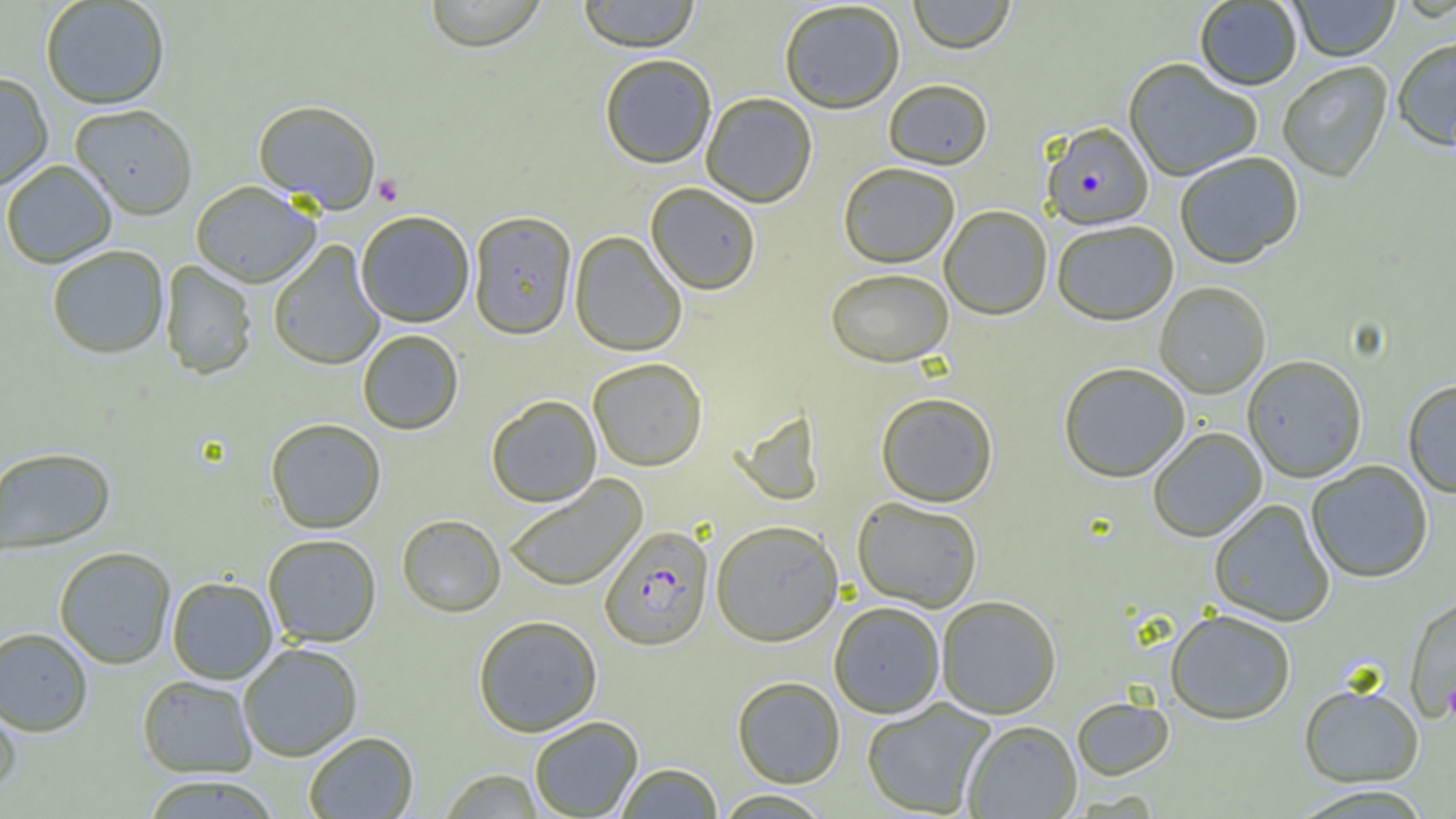
Summary:
  - Coordinate format: approximate bounding boxes as (x1,y1)-(x2,y2) corner pairs in pixels
  - Plasmodium falciparum-infected red blood cell locations: (1042,123)-(1154,232), (600,526)-(714,652)
  - Platelet locations: (373,173)-(404,207), (1442,680)-(1456,723)
  - Uninfected red blood cell locations: (423,0)-(548,53), (576,0)-(701,54), (908,0)-(1016,56), (1290,0)-(1400,63), (40,1)-(170,111), (779,2)-(906,116), (1194,2)-(1302,92), (1393,40)-(1456,155), (600,56)-(716,170), (1123,60)-(1262,182), (1278,63)-(1393,184), (0,73)-(53,192), (884,82)-(993,172), (701,94)-(817,209), (252,100)-(382,213), (70,106)-(197,221), (1175,153)-(1304,269), (1,161)-(117,269), (838,165)-(960,270), (191,183)-(320,289), (645,184)-(761,298), (940,207)-(1052,322), (356,212)-(474,328), (468,213)-(577,342), (1052,222)-(1179,328), (569,232)-(687,358), (268,241)-(385,371), (47,246)-(169,360), (160,261)-(257,381), (825,270)-(953,369), (1155,283)-(1270,400), (357,330)-(464,435), (1242,356)-(1367,484), (588,359)-(707,472), (1058,364)-(1190,483), (1402,380)-(1456,499), (875,394)-(998,508), (486,395)-(602,508), (733,411)-(824,508), (265,418)-(386,534), (1148,428)-(1267,543), (1,447)-(116,556), (1307,461)-(1433,584), (504,475)-(648,592), (852,498)-(982,613), (1209,499)-(1335,627), (397,515)-(506,618), (710,521)-(843,648), (263,534)-(382,648), (54,547)-(176,669), (167,577)-(278,684), (1404,593)-(1456,724), (936,597)-(1062,719), (829,602)-(945,718), (1165,611)-(1296,726), (473,616)-(602,738), (0,627)-(93,737), (238,643)-(363,762), (137,675)-(257,778), (732,676)-(845,789), (1299,685)-(1424,788), (0,696)-(22,798), (1072,697)-(1174,781), (861,699)-(995,817), (529,717)-(644,818), (963,721)-(1082,818), (303,731)-(419,818), (615,763)-(723,818), (438,769)-(543,818), (140,775)-(281,819), (1289,785)-(1434,818), (712,790)-(834,818)
  - Slide-level diagnosis: Plasmodium falciparum
  - Magnification: 1000x
  - Image size: 1456×819 pixels
  - Preparation: thin blood film
  - Modality: optical microscopy
  - Field of view: single